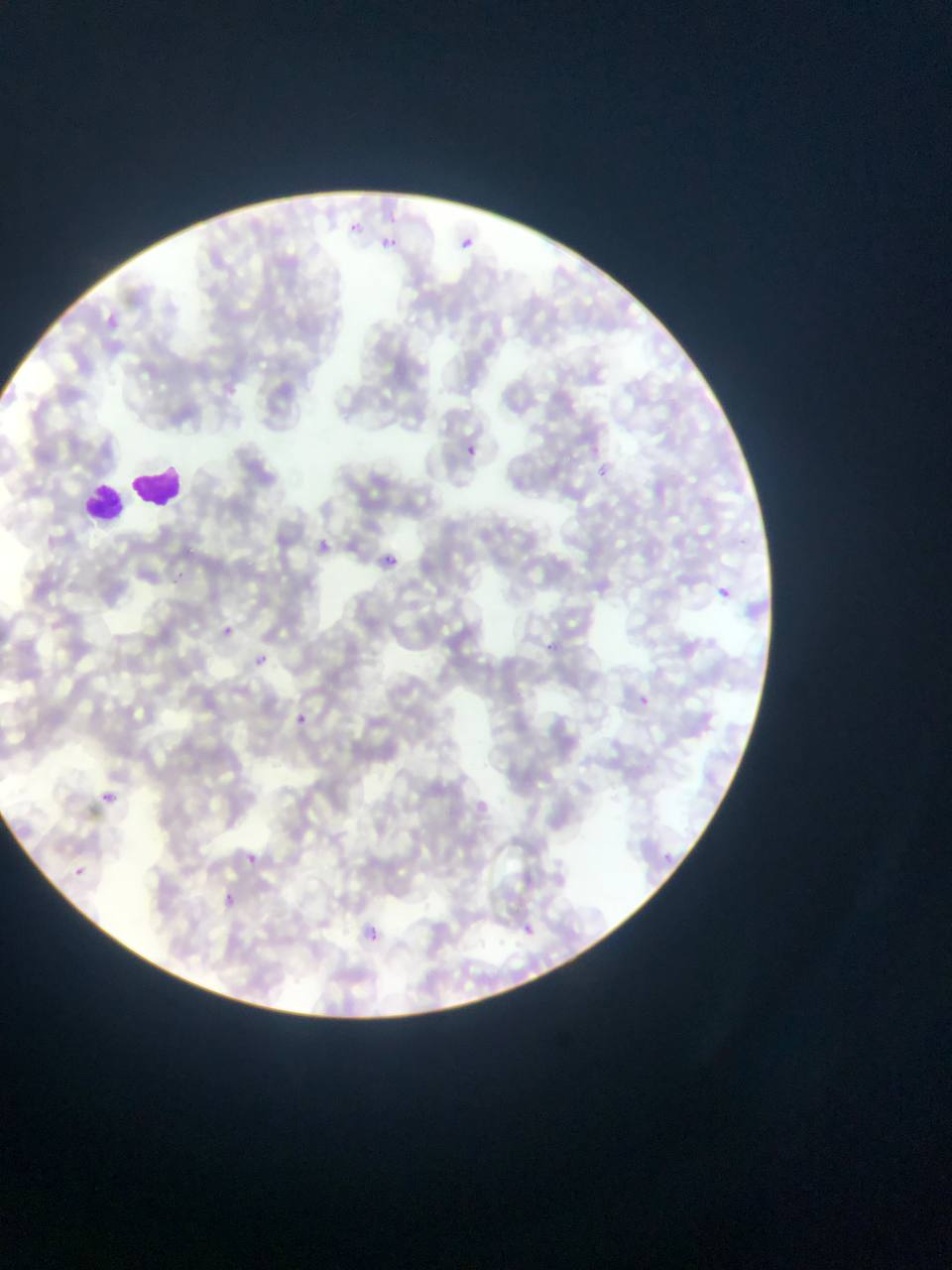

Approximate bounding boxes as left top right bottom in pixels. Leukocyte locations: 132 464 184 508; 104 470 176 523; 83 478 128 517. Plasmodium parasite locations: 380 209 399 226; 348 218 361 232; 463 234 475 251; 381 236 398 248; 465 444 477 458; 597 464 610 477; 314 531 331 556; 383 553 403 569; 168 569 187 586; 716 587 731 599; 219 627 236 639; 544 636 554 654; 255 654 265 664; 631 691 650 708; 292 710 313 731; 103 791 116 804; 244 846 265 866; 661 848 678 863; 73 866 85 876; 221 892 238 913; 367 923 390 948; 524 924 535 934. Thin blood smear. Image is 952×1270 pixels. Single field of view. Collected in Ghana. Mobile-phone photograph taken through the microscope.